Find the cells and give the type of each one.
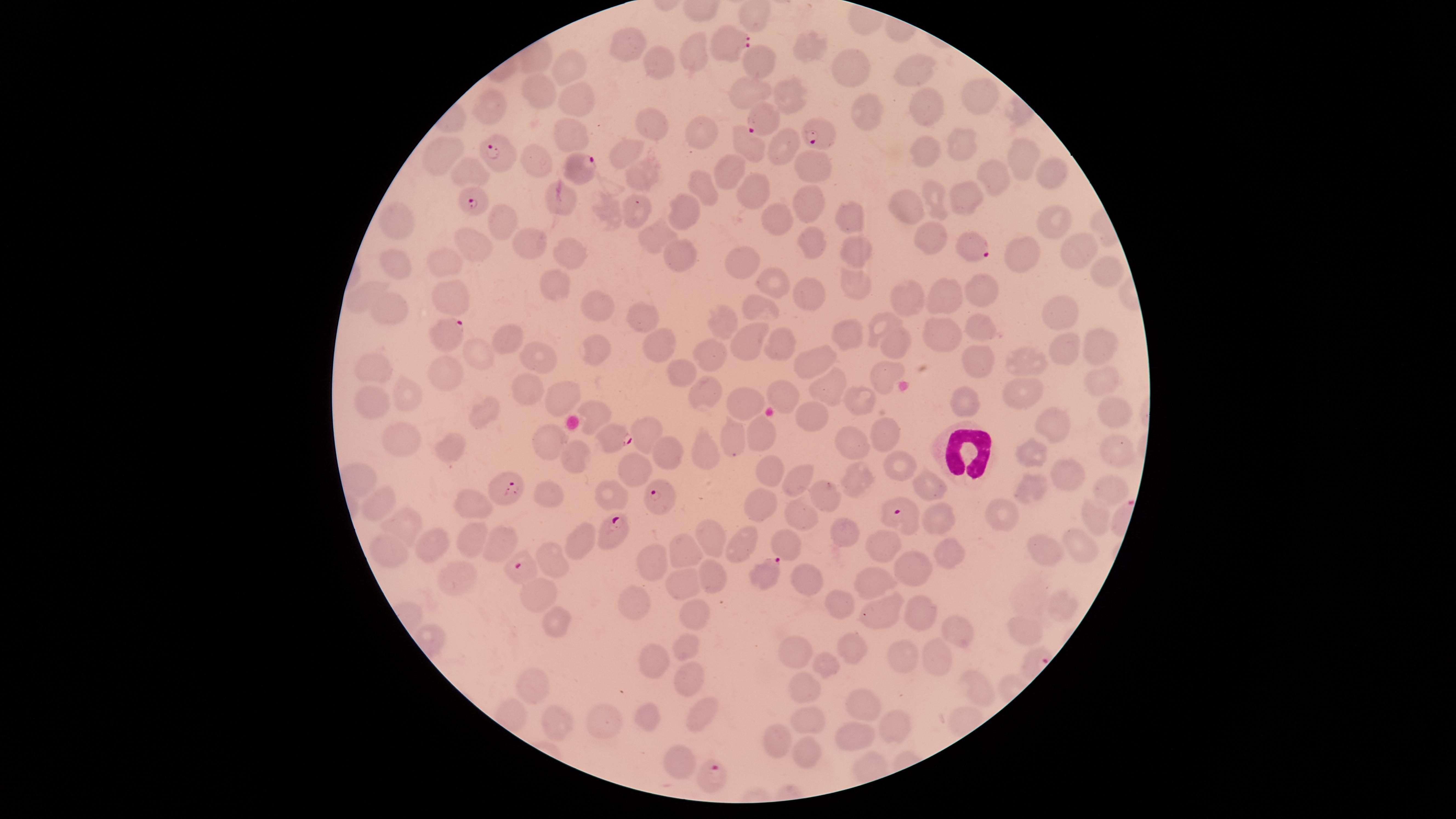
Approximate marker points, in pixels from the top-left corner.
Parasitized red blood cells: (x=733, y=47), (x=763, y=121), (x=821, y=129), (x=503, y=154), (x=581, y=168), (x=482, y=198), (x=975, y=244), (x=445, y=335), (x=613, y=429), (x=501, y=482), (x=660, y=492), (x=900, y=512), (x=608, y=532), (x=524, y=567), (x=765, y=572), (x=711, y=777).
Uninfected red blood cells: (x=627, y=42), (x=811, y=50), (x=698, y=55), (x=757, y=59), (x=850, y=64), (x=570, y=65), (x=659, y=68), (x=921, y=71), (x=792, y=89), (x=744, y=93), (x=973, y=95), (x=542, y=96), (x=576, y=101), (x=484, y=112), (x=919, y=112), (x=859, y=117), (x=654, y=127), (x=702, y=132), (x=570, y=134), (x=953, y=144), (x=444, y=145), (x=785, y=146), (x=748, y=148), (x=630, y=150), (x=922, y=150), (x=1021, y=157), (x=539, y=160), (x=466, y=167), (x=809, y=167), (x=1051, y=168), (x=728, y=170), (x=649, y=176), (x=991, y=177), (x=704, y=184), (x=751, y=193), (x=974, y=196), (x=561, y=202), (x=940, y=202), (x=636, y=203), (x=807, y=204), (x=910, y=205), (x=693, y=211), (x=1056, y=213), (x=846, y=217), (x=507, y=222), (x=778, y=222), (x=398, y=224), (x=644, y=235), (x=928, y=238), (x=469, y=239), (x=533, y=239), (x=815, y=241), (x=1073, y=246), (x=852, y=249), (x=682, y=250), (x=1019, y=250), (x=571, y=254), (x=737, y=262), (x=397, y=267), (x=449, y=270), (x=1109, y=275), (x=550, y=280), (x=856, y=281), (x=776, y=283), (x=985, y=288), (x=807, y=295), (x=363, y=297), (x=950, y=298), (x=911, y=299), (x=451, y=300), (x=390, y=304), (x=756, y=305), (x=1062, y=310), (x=595, y=311), (x=724, y=316), (x=647, y=317), (x=883, y=325), (x=980, y=328), (x=850, y=329), (x=938, y=330), (x=1096, y=339), (x=511, y=341), (x=748, y=341), (x=784, y=344), (x=899, y=344), (x=1067, y=348), (x=600, y=350), (x=662, y=350), (x=976, y=350), (x=478, y=353), (x=547, y=353), (x=713, y=355), (x=819, y=356), (x=1028, y=364), (x=378, y=365), (x=686, y=370), (x=886, y=373), (x=453, y=374), (x=831, y=384), (x=1105, y=384), (x=703, y=390), (x=525, y=392), (x=787, y=392), (x=1027, y=393), (x=409, y=395), (x=863, y=399), (x=970, y=399), (x=563, y=400), (x=372, y=401), (x=596, y=408), (x=748, y=408), (x=1115, y=410), (x=482, y=411), (x=815, y=419), (x=1053, y=422), (x=645, y=432), (x=757, y=432), (x=883, y=432), (x=402, y=438), (x=733, y=438), (x=550, y=442), (x=452, y=445), (x=854, y=446), (x=708, y=450), (x=1116, y=450), (x=577, y=453), (x=662, y=454), (x=1032, y=456), (x=898, y=463), (x=630, y=467), (x=768, y=470), (x=1072, y=471), (x=796, y=477), (x=862, y=482), (x=1034, y=483), (x=929, y=487), (x=1112, y=488), (x=552, y=489), (x=608, y=494), (x=826, y=498), (x=471, y=502), (x=379, y=503), (x=765, y=508), (x=1096, y=516), (x=799, y=517), (x=1006, y=517), (x=942, y=518), (x=407, y=524), (x=844, y=530), (x=468, y=535), (x=711, y=537), (x=783, y=539), (x=501, y=540), (x=584, y=542), (x=742, y=542), (x=439, y=543), (x=1076, y=543), (x=689, y=546), (x=948, y=547), (x=1042, y=549), (x=394, y=550), (x=882, y=551), (x=550, y=552), (x=647, y=558), (x=715, y=569), (x=914, y=570), (x=453, y=576), (x=806, y=578), (x=873, y=581), (x=689, y=583), (x=541, y=590), (x=1031, y=592), (x=631, y=598), (x=835, y=602), (x=1063, y=605), (x=690, y=612), (x=919, y=612), (x=878, y=613), (x=554, y=618), (x=1021, y=629), (x=950, y=632), (x=685, y=645), (x=852, y=645), (x=790, y=648), (x=652, y=655), (x=906, y=657), (x=937, y=657), (x=831, y=662), (x=688, y=677), (x=806, y=683), (x=977, y=684), (x=535, y=689), (x=872, y=712), (x=699, y=714), (x=652, y=717), (x=606, y=719), (x=810, y=724), (x=892, y=724), (x=556, y=725), (x=859, y=734), (x=778, y=744), (x=804, y=746), (x=678, y=756).
White blood cells: (x=963, y=449).

visible region = circular
species = Plasmodium falciparum
capture = smartphone photograph through the microscope eyepiece
stain = Giemsa
preparation = thin blood film
image size = 1456×819 pixels
field of view = single